Assess this cell for malaria.
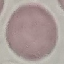
It is uninfected.

Giemsa stain. Photographed with a smartphone camera at the microscope eyepiece. Automatically extracted cell patch, resized to 64 × 64 pixels. Thin smear of blood.